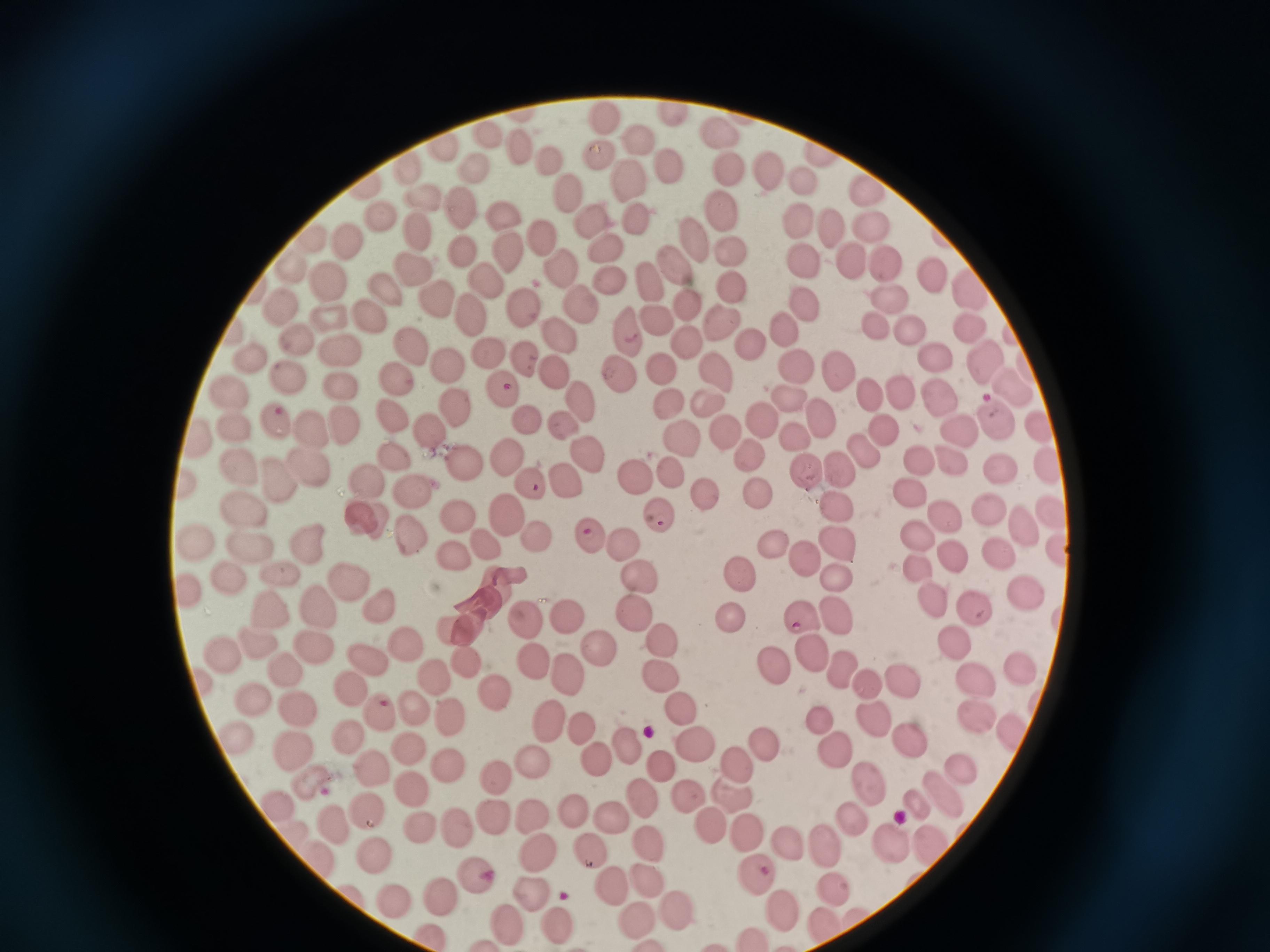
{
  "cell_locations": "approximate centers as [x, y] in pixels: [672, 115], [607, 119], [722, 128], [639, 137], [605, 153], [551, 161], [669, 168], [728, 168], [770, 169], [802, 179], [630, 181], [869, 188], [566, 199], [424, 203], [726, 207], [463, 212], [381, 213], [637, 215], [794, 216], [503, 220], [588, 225], [870, 228], [825, 231], [418, 233], [542, 236], [696, 238], [350, 239], [604, 246], [733, 249], [466, 254], [511, 258], [888, 259], [849, 260], [673, 261], [805, 267], [292, 269], [558, 271], [931, 273], [607, 276], [413, 277], [647, 277], [331, 281], [491, 282], [733, 285], [965, 285], [389, 293], [428, 294], [888, 297], [685, 305], [802, 305], [579, 309], [279, 311], [371, 311], [523, 312], [329, 315], [650, 317], [471, 320], [719, 322], [871, 324], [783, 325], [912, 330], [623, 331], [969, 332], [1010, 333], [554, 334], [298, 339], [684, 342], [749, 344], [414, 350], [932, 351], [341, 354], [525, 354], [250, 356], [490, 356], [981, 358], [444, 360], [661, 366], [792, 366], [836, 368], [618, 372], [717, 372], [288, 377], [553, 377], [397, 382], [1008, 383], [501, 387], [342, 391], [941, 394], [865, 395], [896, 395], [233, 397], [785, 398], [579, 402], [666, 402], [705, 402], [453, 406], [280, 414], [821, 415], [765, 419], [528, 420], [391, 421], [560, 426], [232, 427], [994, 427], [342, 428], [961, 428], [1038, 429], [430, 430], [314, 432], [882, 433], [722, 435], [797, 435], [677, 442], [202, 443], [860, 452], [584, 453], [503, 454], [749, 455], [949, 456], [395, 458], [461, 458], [919, 462], [1052, 464], [239, 467], [313, 469], [998, 470], [838, 471], [634, 472], [669, 472], [804, 472], [180, 478], [562, 481], [527, 485], [273, 486], [366, 486], [910, 491], [758, 492], [416, 494], [711, 496], [1051, 506], [837, 507], [502, 510], [985, 510], [246, 513], [654, 513], [942, 514], [459, 519], [368, 521], [1026, 529], [587, 536], [542, 537], [915, 538], [198, 541], [412, 541], [303, 542], [488, 542], [624, 543], [774, 544], [836, 544], [1057, 549], [253, 553], [458, 557], [951, 557], [998, 559], [801, 561], [913, 567], [740, 572], [187, 577], [346, 577], [637, 578], [833, 579], [235, 581], [282, 583], [1025, 596], [933, 600], [485, 604], [318, 606], [632, 610], [967, 610], [380, 612], [268, 614], [836, 615], [569, 617], [803, 617], [728, 620], [526, 622], [452, 633], [661, 641], [253, 644], [315, 644], [406, 644], [955, 644], [600, 648], [812, 651], [218, 652], [530, 654], [361, 659], [471, 662], [778, 663], [841, 667], [1020, 667], [289, 669], [971, 675], [569, 676], [662, 676], [202, 677], [432, 678], [903, 679], [870, 685], [494, 690], [358, 692], [257, 698], [681, 709], [294, 710], [418, 711], [971, 712], [379, 714], [447, 715], [822, 720], [547, 721], [873, 722], [234, 729], [582, 729], [1012, 730], [353, 739], [907, 740], [692, 743], [630, 744], [764, 745], [296, 747], [833, 748], [412, 750], [594, 759], [535, 762], [957, 763], [736, 764], [659, 765], [449, 769], [375, 776], [498, 777], [316, 781], [865, 782], [410, 788], [944, 790], [642, 794], [736, 796], [687, 799], [273, 803], [917, 803], [574, 806], [360, 811], [492, 813], [529, 815], [854, 816], [614, 818], [328, 821], [417, 825], [714, 828], [456, 829], [747, 837], [889, 839], [786, 840], [925, 844], [827, 845], [649, 846], [539, 851], [592, 852], [377, 854], [316, 857], [755, 870], [479, 880], [647, 880], [618, 886], [533, 889], [835, 891], [440, 894], [393, 902], [779, 907], [679, 912], [641, 919], [556, 924], [512, 927]",
  "image_size": "1270×952 pixels",
  "preparation": "thin smear",
  "field_of_view": "single",
  "capture": "smartphone camera at the microscope eyepiece",
  "stain": "Giemsa"
}